Assess for Plasmodium parasites.
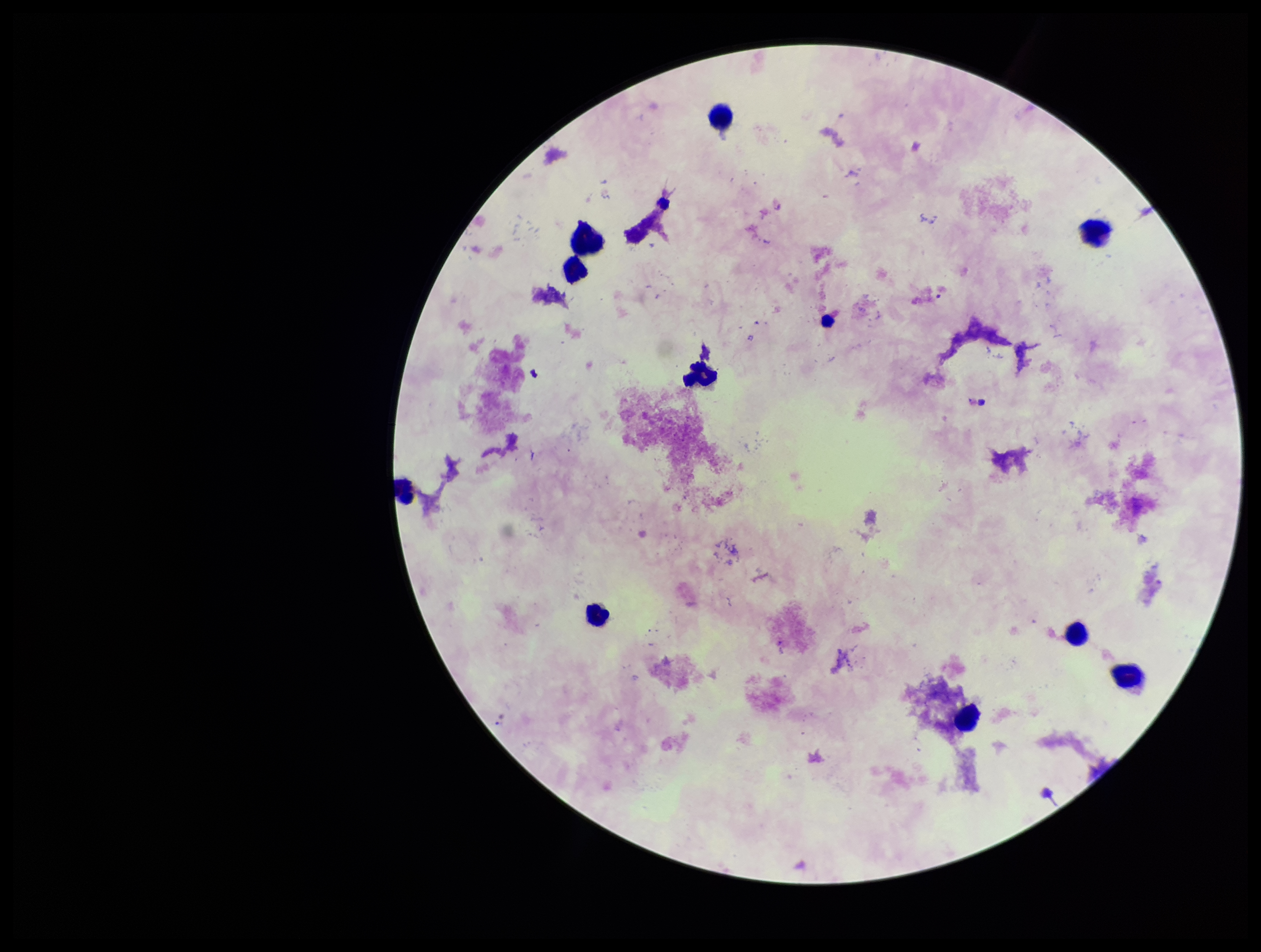

None identified.

Preparation: thick. Image is 1261×952 pixels. Parasite count: 0. Leukocyte count: 10. Smartphone photograph taken through the eyepiece of a microscope. Single field of view. Stained with Giemsa. Patient malaria status: negative.